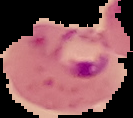
Summary:
  - Preparation: thin blood film
  - Image type: segmented cell region on a black background
  - Malaria status: parasitized
  - Image size: 133×118 pixels